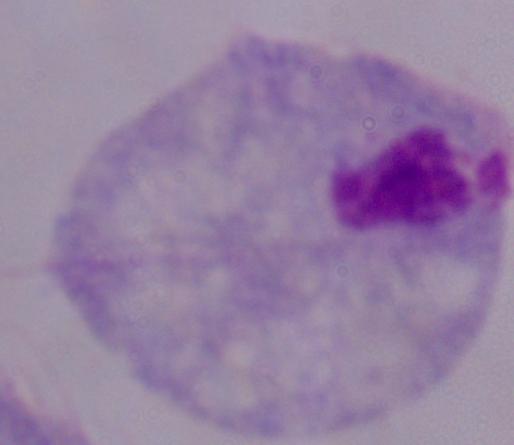
identification = trichomonad
magnification = 1000x
modality = photomicrograph